Classify this cell by malaria status.
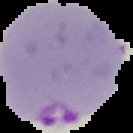

It is parasitized.

Cell region segmented out of the field of view; the surrounding area is masked to black. From a thin blood smear. Image is 133×133 pixels.